Identify the cell.
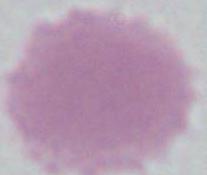

This is an erythrocyte.

magnification = 1000x
modality = photomicrograph